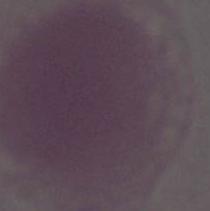
modality: micrograph
identification: erythrocyte
magnification: 1000x